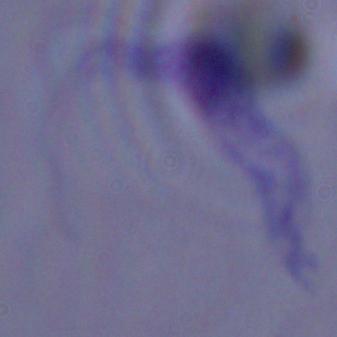
magnification = 1000x
identification = trypanosome
modality = micrograph